Assess this cell for malaria.
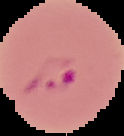
Parasitized.

{
  "image_type": "segmented cell region with the area outside set to black",
  "image_size": "124×136 pixels",
  "preparation": "thin blood smear"
}